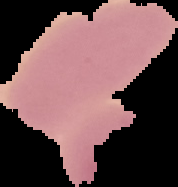

Malaria status: uninfected. Segmented cell region on a black background. From a thin blood smear. Image is 178×187 pixels.